Assess the morphology of the red blood cells.
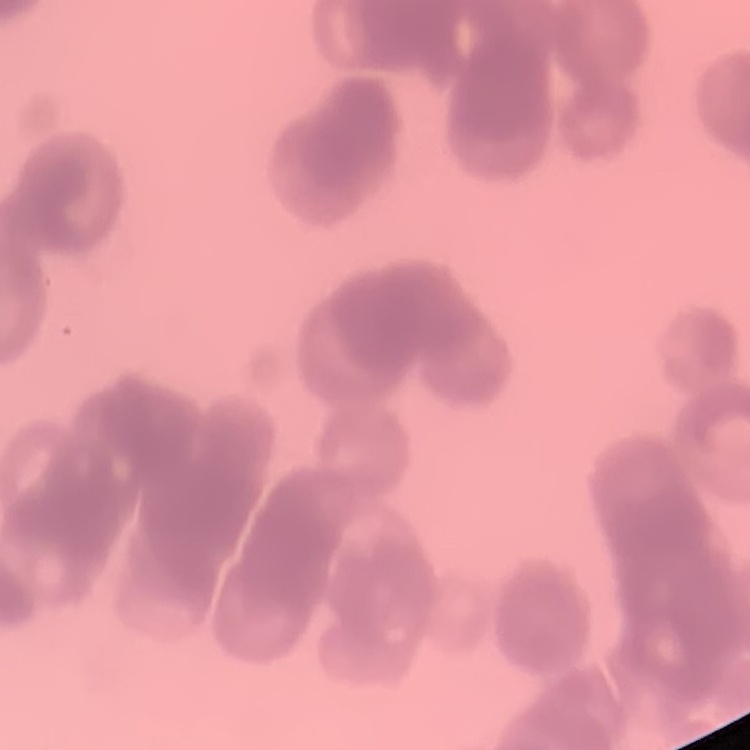

Rouleaux formation.

Summary:
  - Preparation: thin blood film
  - Image type: one tile cut from a larger photomicrograph
  - Stain: Field's or Giemsa